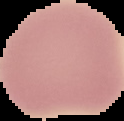
Summary:
  - Image type: segmented cell region on a black background
  - Preparation: thin blood film
  - Result: negative for Plasmodium parasites
  - Image size: 124×121 pixels